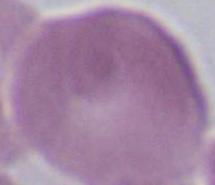 Captured at 1000x magnification. Photomicrograph. A red blood cell is shown.